Assess the morphology of the red blood cells.
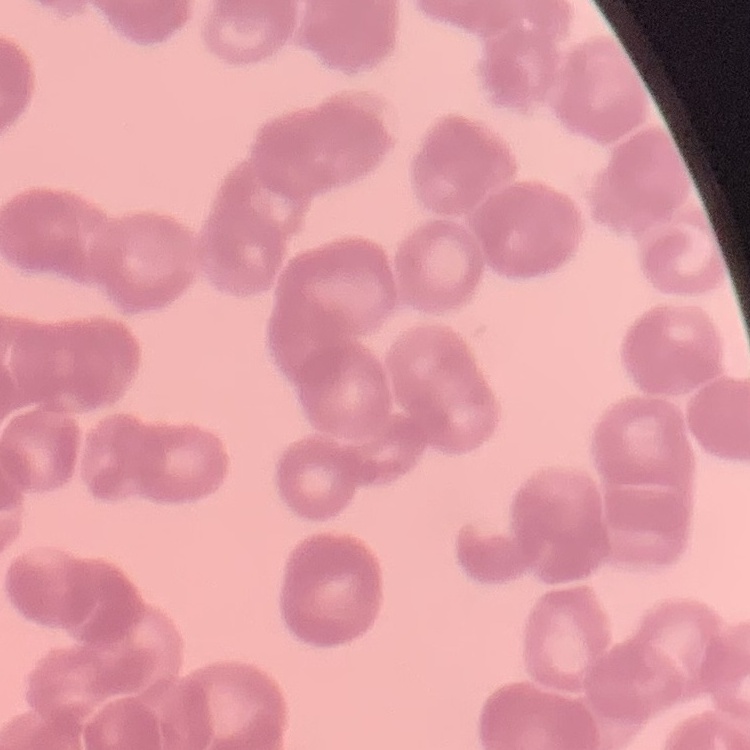
They show rouleaux formation.

Summary:
  - Preparation: thin peripheral smear
  - Image type: square crop of a larger photomicrograph
  - Stain: Field's or Giemsa